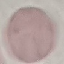 Malaria status: uninfected. Thin smear of blood. Automatically extracted cell patch, resized to 64 × 64 pixels. Photographed with a smartphone camera at the microscope eyepiece. Giemsa-stained preparation.